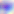
magnification: 400x
modality: micrograph
identification: Toxoplasma gondii